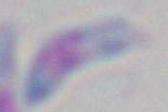 Micrograph. Captured at 1000x magnification. Toxoplasma gondii is shown.